Find the red blood cells and label each as Plasmodium falciparum-infected, uninfected, or of indeterminate infection status.
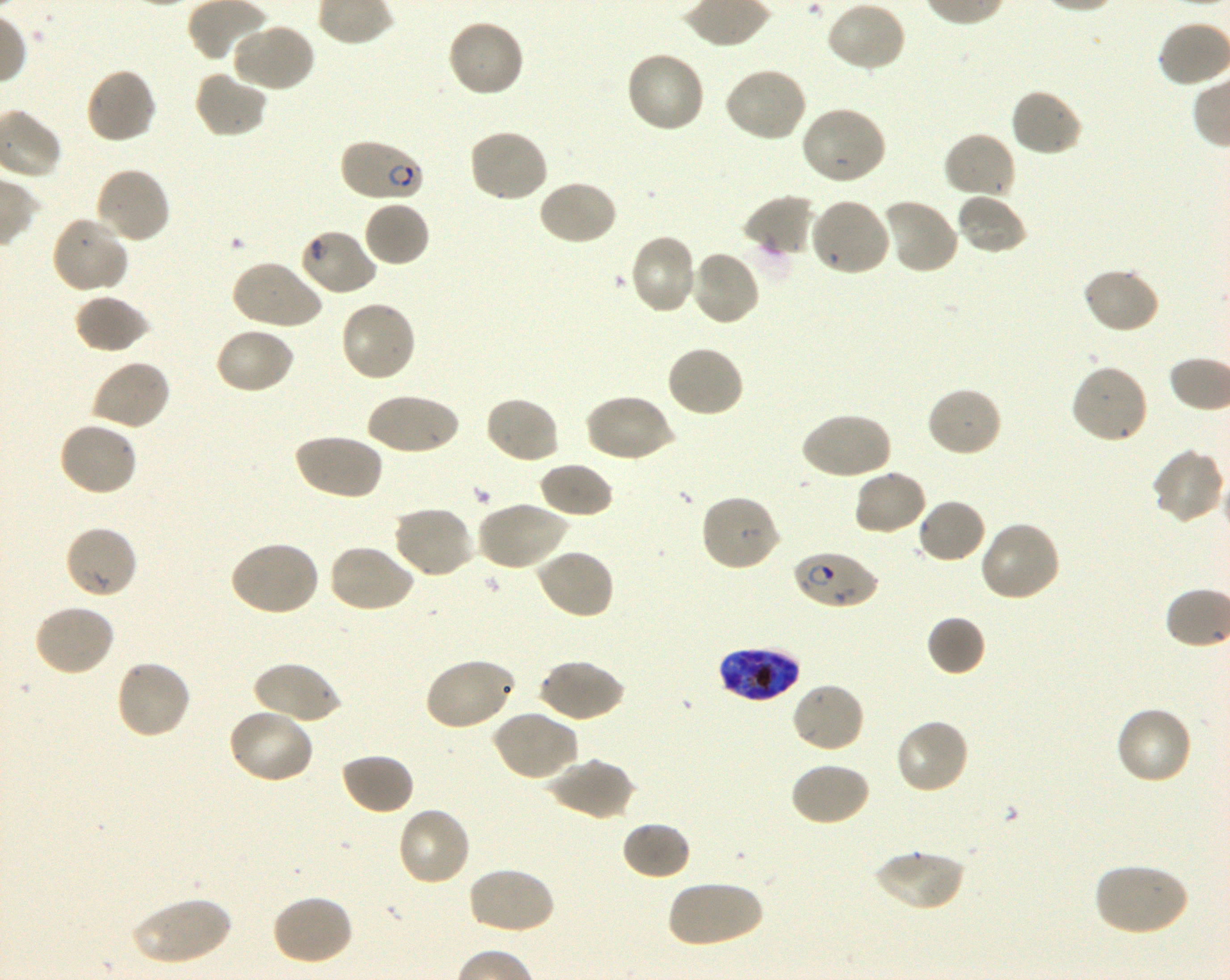

Approximate bounding boxes as [x1, y1, x2, y2] in pixels. Not every red blood cell is marked. A life-cycle stage — or a range of stages, where the recorded stages span more than one — follows each staged infected red blood cell.
Infected red blood cells: [338, 137, 425, 204] ring; [792, 549, 878, 611] ring; [718, 645, 800, 702] late trophozoite to late schizont.
Red blood cells of indeterminate infection status: [298, 227, 377, 296].
Uninfected red blood cells: [825, 1, 908, 74], [445, 18, 525, 100], [229, 22, 317, 94], [624, 50, 706, 134], [722, 66, 809, 142], [85, 67, 158, 144], [193, 71, 268, 139], [1009, 88, 1083, 157], [800, 106, 888, 186], [467, 128, 550, 203], [941, 131, 1018, 201], [95, 166, 171, 245], [537, 179, 618, 247], [955, 192, 1028, 255], [741, 194, 816, 261], [809, 197, 892, 278], [881, 198, 960, 276], [363, 200, 431, 268], [51, 215, 130, 296], [628, 232, 699, 316], [688, 249, 761, 327], [230, 259, 323, 331], [1082, 266, 1160, 334], [74, 292, 150, 354], [338, 299, 417, 383], [213, 326, 295, 395], [665, 345, 746, 419], [91, 359, 171, 431], [1070, 363, 1150, 445], [926, 386, 1003, 458], [364, 392, 461, 456], [583, 392, 675, 464], [484, 395, 561, 465], [800, 410, 892, 481], [57, 420, 139, 497], [292, 432, 383, 501], [1150, 447, 1227, 525], [538, 461, 615, 520], [852, 468, 928, 536], [699, 494, 781, 573], [915, 498, 987, 565], [476, 499, 569, 571], [392, 505, 476, 579], [979, 521, 1062, 604], [63, 525, 139, 600], [228, 540, 320, 618], [327, 543, 417, 614], [535, 548, 615, 621], [32, 603, 115, 677], [927, 615, 986, 677], [422, 658, 515, 732], [538, 658, 625, 723], [114, 659, 192, 741], [253, 661, 341, 726], [790, 681, 866, 755], [1113, 705, 1193, 786], [226, 708, 314, 785], [490, 710, 577, 782], [894, 718, 970, 795], [339, 752, 415, 815], [547, 757, 635, 821], [788, 761, 870, 827], [396, 807, 472, 888], [620, 820, 692, 880], [873, 848, 965, 912], [1092, 862, 1190, 937], [467, 865, 556, 936], [666, 879, 762, 948], [270, 894, 354, 966], [127, 897, 234, 966].

100x oil-immersion objective, numerical aperture 1.30. Giemsa-stained preparation. Image is 1230×980 pixels. Thin blood film. Shaking in-vitro culture of Plasmodium falciparum strain 3D7. Blood group of the donor: O+. Single field of view.